Identify the parasite.
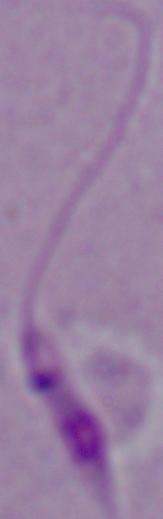

Leishmania.

magnification = 1000x
modality = micrograph